Locate every blood parasite and identify its species.
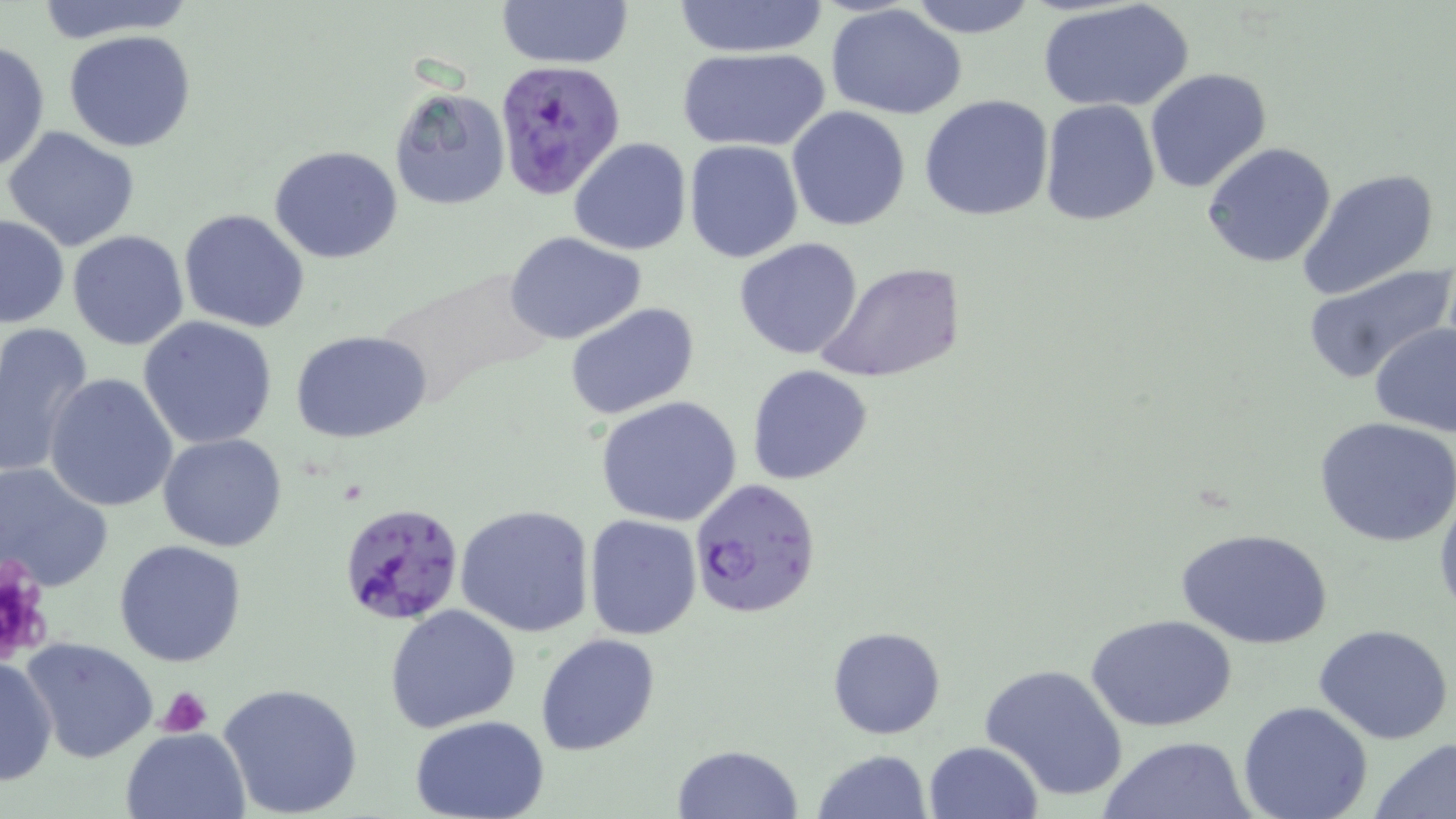

Approximate bounding boxes as (x1, y1, x2, y2) in pixels.
Plasmodium falciparum-infected red blood cells: (495, 60, 624, 200), (687, 476, 821, 620), (335, 500, 464, 629).
No Plasmodium ovale, Plasmodium malariae, Plasmodium vivax, Babesia divergens, or Trypanosoma brucei observed.

Platelet locations: (0, 557, 56, 668), (156, 684, 214, 736). Uninfected red blood cell locations: (30, 0, 200, 42), (495, 0, 633, 69), (903, 0, 1043, 38), (1040, 0, 1195, 113), (671, 1, 829, 57), (826, 4, 968, 120), (65, 29, 197, 153), (0, 41, 50, 177), (677, 47, 830, 152), (1143, 67, 1273, 193), (389, 86, 510, 211), (919, 94, 1056, 222), (1040, 99, 1160, 226), (787, 106, 911, 230), (3, 124, 141, 253), (570, 136, 692, 255), (684, 140, 803, 263), (1201, 142, 1337, 268), (269, 145, 405, 263), (1296, 168, 1441, 298), (177, 208, 310, 332), (1, 213, 68, 328), (68, 229, 191, 350), (504, 231, 648, 345), (733, 236, 864, 359), (1304, 261, 1453, 380), (819, 262, 965, 385), (376, 266, 557, 411), (565, 303, 699, 422), (139, 316, 278, 448), (0, 321, 94, 481), (1369, 322, 1456, 438), (291, 330, 433, 444), (747, 364, 874, 484), (43, 372, 179, 512), (594, 396, 743, 526), (1314, 416, 1456, 547), (158, 433, 288, 552), (0, 461, 111, 591), (1433, 485, 1456, 624), (454, 503, 595, 636), (584, 515, 702, 640), (1174, 527, 1334, 649), (114, 539, 247, 667), (385, 604, 521, 735), (1088, 614, 1239, 733), (1313, 623, 1453, 745), (827, 625, 946, 739), (535, 633, 660, 756), (22, 637, 158, 763), (0, 654, 58, 788), (980, 663, 1133, 804), (219, 680, 366, 819), (1238, 700, 1374, 819), (411, 714, 550, 819), (120, 728, 251, 818), (1100, 734, 1254, 818), (1372, 739, 1456, 818), (923, 740, 1044, 819), (671, 743, 803, 818), (810, 749, 932, 819). Slide-level diagnosis: Plasmodium falciparum. One field of a larger specimen. Optical microscopy. Image is 1456×819 pixels. Thin blood smear. 1000x magnification. May-Grünwald-Giemsa stain.